Assess the morphology of the red blood cells.
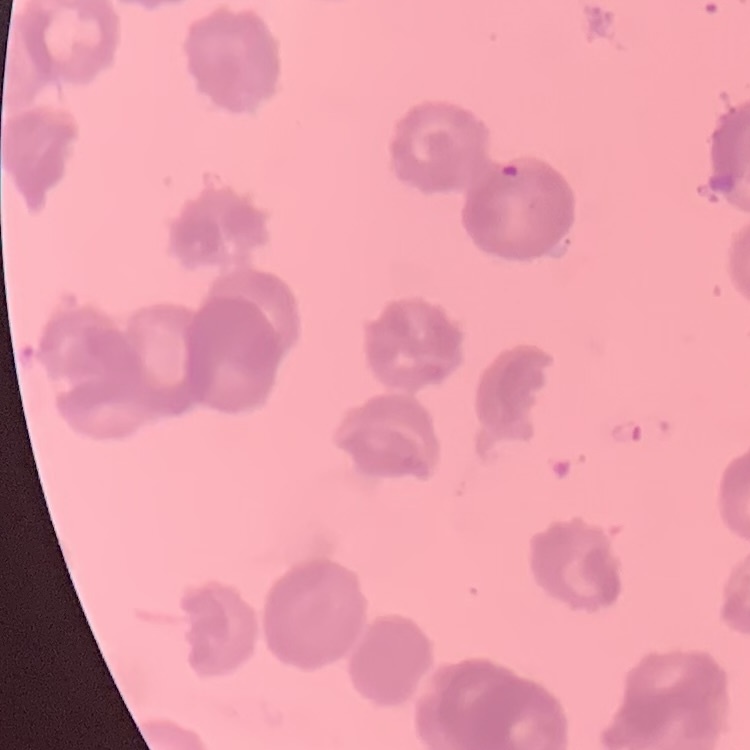

They show rouleaux formation.

stain = Field's or Giemsa
preparation = thin peripheral smear
image type = one tile cut from a larger photomicrograph